Outline each Plasmodium falciparum-infected red blood cell.
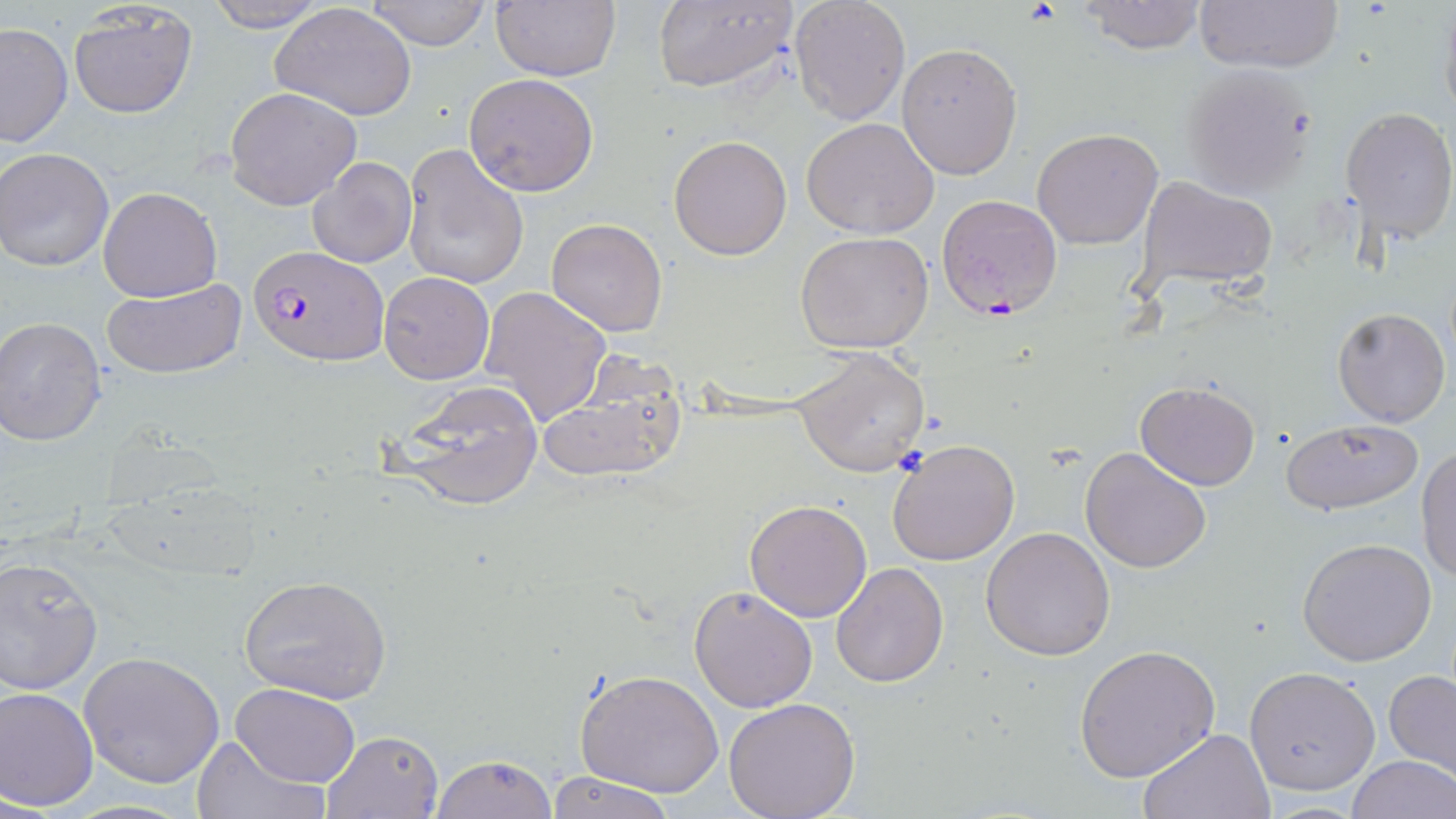
Approximate bounding boxes as (x1,y1)-(x2,y2) corner pairs in pixels.
Plasmodium falciparum-infected red blood cells: (936,193)-(1064,321), (249,246)-(387,367).

Uninfected red blood cell locations: (203,0)-(331,33), (364,0)-(492,49), (491,0)-(620,82), (788,0)-(910,124), (1076,0)-(1208,54), (1192,0)-(1344,74), (1438,0)-(1456,129), (651,1)-(796,93), (69,3)-(197,118), (272,3)-(417,121), (1,22)-(73,147), (896,41)-(1022,180), (1179,63)-(1317,198), (465,72)-(600,196), (226,88)-(363,211), (1342,107)-(1456,244), (802,118)-(940,239), (1033,127)-(1165,249), (668,134)-(793,259), (402,143)-(530,292), (1,147)-(114,272), (307,158)-(416,270), (1133,175)-(1279,292), (97,186)-(221,301), (546,217)-(668,337), (793,232)-(936,354), (378,271)-(494,385), (99,276)-(246,380), (479,285)-(612,428), (1333,307)-(1450,427), (0,316)-(108,447), (793,348)-(930,478), (536,362)-(686,486), (387,378)-(546,513), (1134,382)-(1260,490), (1280,417)-(1424,516), (887,438)-(1021,567), (1416,444)-(1456,585), (1080,446)-(1212,572), (745,500)-(873,622), (980,528)-(1115,662), (1298,537)-(1441,666), (0,557)-(103,695), (830,563)-(949,687), (238,574)-(391,704), (689,587)-(819,713), (1074,644)-(1220,781), (78,651)-(226,788), (1245,666)-(1381,796), (574,668)-(725,798), (1383,669)-(1456,778), (231,683)-(361,786), (0,685)-(99,810), (720,698)-(862,819), (1138,727)-(1277,818), (322,729)-(445,818), (191,735)-(326,819), (432,753)-(558,819), (1347,755)-(1455,819), (544,772)-(675,818). Slide-level diagnosis: Plasmodium falciparum. Image is 1456×819 pixels. Captured at 1000x magnification. Single field of view. May-Grünwald-Giemsa stain. Thin blood film. Optical microscopy.